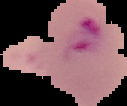

Summary:
  - Image size: 127×106 pixels
  - Image type: cell region segmented out of the field of view; surrounding area masked to black
  - Result: malaria parasites detected
  - Preparation: thin blood smear